Give the preparation type.
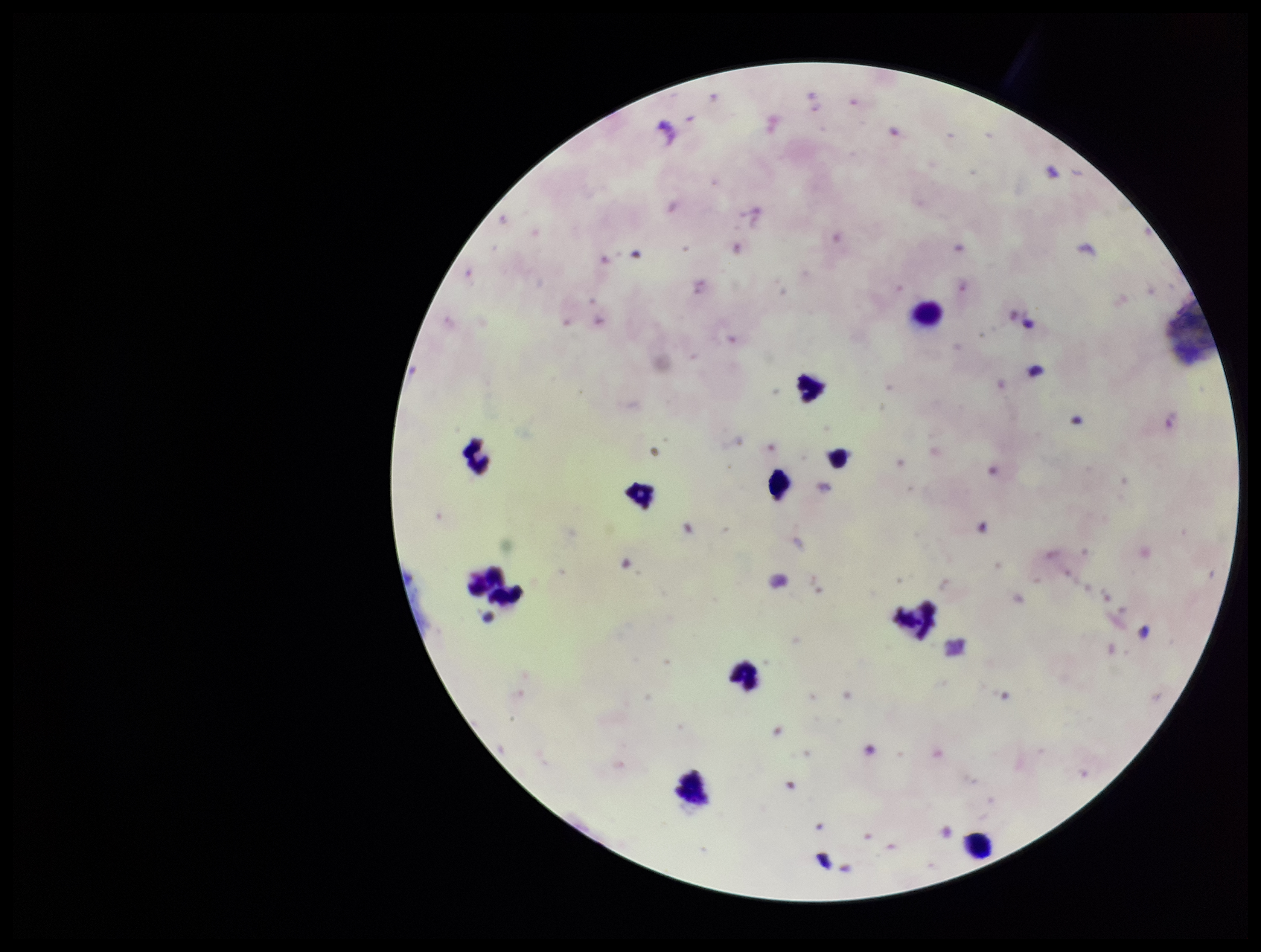

It is a thick blood smear.

leukocyte count = 12
species reported for this patient = Plasmodium falciparum
patient malaria status = positive
capture = smartphone photograph through the microscope eyepiece
stain = Giemsa
field of view = one from this slide
image size = 1261×952 pixels
parasite count = 2
Plasmodium parasites = detected